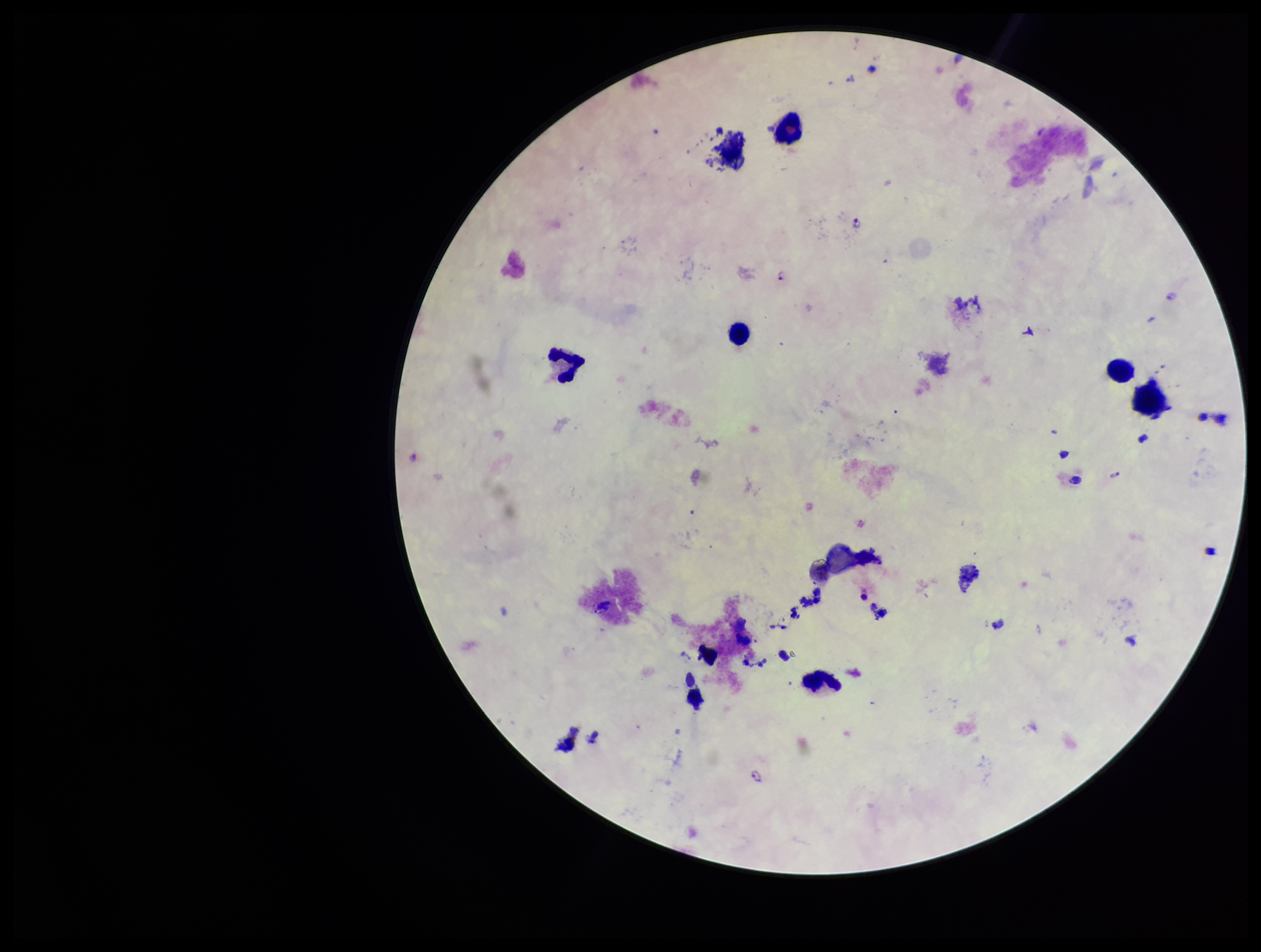
{
  "stain": "Giemsa",
  "leukocyte_count": 6,
  "preparation": "thick",
  "plasmodium_parasites": "identified",
  "image_size": "1261×952 pixels",
  "capture": "smartphone photograph through the microscope eyepiece",
  "species_reported_for_this_patient": "Plasmodium falciparum",
  "parasite_count": 3,
  "patient_malaria_status": "positive",
  "field_of_view": "one from this slide"
}